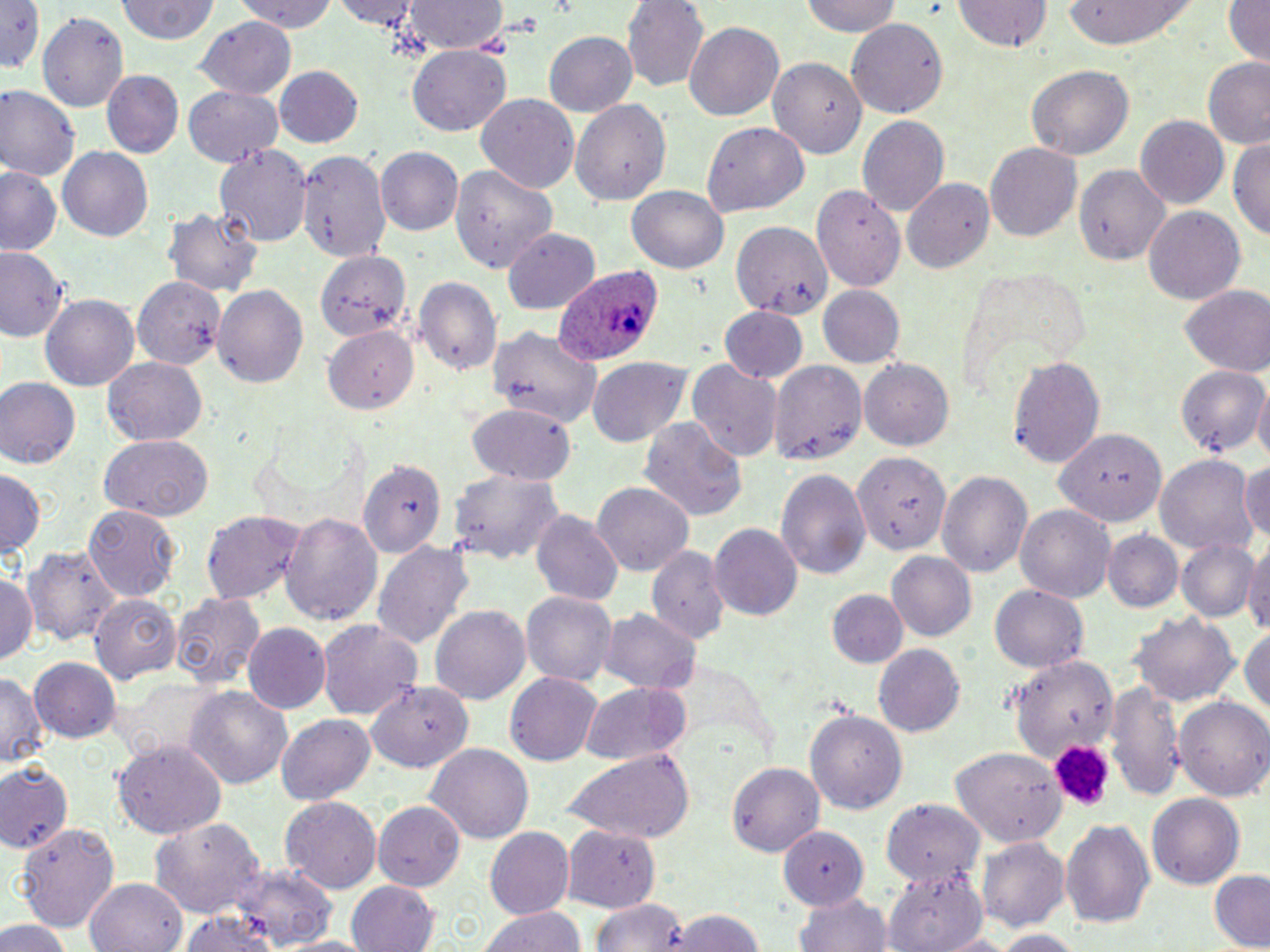

slide-level diagnosis = Plasmodium ovale
stain = May-Grünwald-Giemsa
magnification = 1000x
platelet locations = approximate bounding boxes as named x1/y1/x2/y2 corners in pixels: (x1=1050, y1=737, x2=1116, y2=807)
preparation = thin blood smear
field of view = single
uninfected red blood cell locations = approximate bounding boxes as named x1/y1/x2/y2 corners in pixels: (x1=231, y1=0, x2=341, y2=33), (x1=336, y1=0, x2=421, y2=32), (x1=406, y1=0, x2=508, y2=56), (x1=801, y1=0, x2=902, y2=39), (x1=957, y1=0, x2=1051, y2=55), (x1=1061, y1=0, x2=1200, y2=47), (x1=1221, y1=0, x2=1270, y2=65), (x1=115, y1=1, x2=220, y2=46), (x1=622, y1=1, x2=709, y2=90), (x1=0, y1=3, x2=48, y2=77), (x1=37, y1=12, x2=129, y2=113), (x1=196, y1=17, x2=295, y2=97), (x1=847, y1=18, x2=949, y2=116), (x1=685, y1=20, x2=784, y2=123), (x1=543, y1=31, x2=637, y2=117), (x1=407, y1=46, x2=513, y2=136), (x1=770, y1=58, x2=867, y2=162), (x1=1203, y1=60, x2=1270, y2=149), (x1=1025, y1=65, x2=1134, y2=161), (x1=272, y1=66, x2=365, y2=149), (x1=101, y1=71, x2=181, y2=156), (x1=0, y1=85, x2=82, y2=179), (x1=184, y1=85, x2=284, y2=167), (x1=476, y1=95, x2=579, y2=192), (x1=571, y1=98, x2=671, y2=206), (x1=858, y1=115, x2=949, y2=216), (x1=1136, y1=116, x2=1228, y2=208), (x1=702, y1=122, x2=807, y2=215), (x1=1231, y1=137, x2=1270, y2=243), (x1=215, y1=142, x2=311, y2=244), (x1=985, y1=143, x2=1084, y2=241), (x1=57, y1=146, x2=153, y2=242), (x1=375, y1=147, x2=463, y2=236), (x1=299, y1=148, x2=392, y2=258), (x1=450, y1=163, x2=555, y2=275), (x1=1074, y1=164, x2=1171, y2=267), (x1=0, y1=165, x2=63, y2=257), (x1=900, y1=178, x2=994, y2=275), (x1=627, y1=186, x2=730, y2=274), (x1=811, y1=187, x2=903, y2=293), (x1=165, y1=204, x2=263, y2=299), (x1=1143, y1=207, x2=1246, y2=303), (x1=730, y1=219, x2=831, y2=314), (x1=503, y1=228, x2=599, y2=310), (x1=0, y1=247, x2=68, y2=344), (x1=309, y1=247, x2=414, y2=344), (x1=133, y1=275, x2=226, y2=372), (x1=417, y1=276, x2=500, y2=377), (x1=213, y1=283, x2=308, y2=387), (x1=818, y1=286, x2=906, y2=368), (x1=1180, y1=288, x2=1268, y2=376), (x1=40, y1=294, x2=139, y2=393), (x1=720, y1=306, x2=810, y2=383), (x1=489, y1=324, x2=601, y2=433), (x1=325, y1=328, x2=417, y2=413), (x1=103, y1=355, x2=207, y2=446), (x1=1009, y1=355, x2=1105, y2=469), (x1=588, y1=357, x2=689, y2=448), (x1=860, y1=357, x2=957, y2=450), (x1=688, y1=358, x2=783, y2=464), (x1=770, y1=359, x2=867, y2=466), (x1=1177, y1=363, x2=1270, y2=457), (x1=0, y1=377, x2=79, y2=470), (x1=1252, y1=382, x2=1270, y2=466), (x1=465, y1=405, x2=576, y2=484), (x1=641, y1=417, x2=744, y2=524), (x1=1057, y1=427, x2=1167, y2=530), (x1=97, y1=436, x2=216, y2=520), (x1=855, y1=452, x2=949, y2=553), (x1=1154, y1=455, x2=1256, y2=555), (x1=1244, y1=457, x2=1270, y2=545), (x1=359, y1=458, x2=449, y2=559), (x1=775, y1=466, x2=871, y2=579), (x1=448, y1=467, x2=566, y2=566), (x1=1, y1=469, x2=44, y2=560), (x1=937, y1=469, x2=1033, y2=578), (x1=591, y1=481, x2=693, y2=577), (x1=85, y1=506, x2=180, y2=601), (x1=1016, y1=507, x2=1114, y2=601), (x1=532, y1=509, x2=624, y2=606), (x1=201, y1=511, x2=306, y2=605), (x1=280, y1=511, x2=382, y2=627), (x1=708, y1=521, x2=802, y2=618), (x1=1105, y1=530, x2=1182, y2=611), (x1=1177, y1=538, x2=1257, y2=623), (x1=1244, y1=538, x2=1270, y2=633), (x1=372, y1=540, x2=474, y2=651), (x1=24, y1=544, x2=118, y2=647), (x1=646, y1=546, x2=729, y2=646), (x1=885, y1=552, x2=975, y2=641), (x1=0, y1=572, x2=40, y2=666), (x1=991, y1=585, x2=1089, y2=671), (x1=828, y1=587, x2=907, y2=667), (x1=169, y1=590, x2=267, y2=689), (x1=521, y1=590, x2=617, y2=685), (x1=90, y1=594, x2=181, y2=683), (x1=431, y1=604, x2=530, y2=704), (x1=1133, y1=609, x2=1240, y2=707), (x1=598, y1=610, x2=700, y2=693), (x1=316, y1=616, x2=423, y2=721), (x1=242, y1=624, x2=329, y2=714), (x1=1242, y1=625, x2=1270, y2=722), (x1=873, y1=643, x2=964, y2=737), (x1=1005, y1=654, x2=1116, y2=758), (x1=30, y1=657, x2=121, y2=744), (x1=0, y1=671, x2=46, y2=769), (x1=504, y1=671, x2=602, y2=766), (x1=577, y1=680, x2=689, y2=767), (x1=1103, y1=680, x2=1187, y2=799), (x1=367, y1=681, x2=472, y2=775), (x1=186, y1=685, x2=293, y2=790), (x1=1174, y1=698, x2=1270, y2=800), (x1=805, y1=709, x2=909, y2=813), (x1=275, y1=713, x2=375, y2=804), (x1=113, y1=741, x2=228, y2=839), (x1=425, y1=743, x2=533, y2=845), (x1=559, y1=746, x2=697, y2=844), (x1=951, y1=747, x2=1067, y2=846), (x1=0, y1=762, x2=73, y2=856), (x1=727, y1=764, x2=823, y2=856), (x1=1148, y1=791, x2=1245, y2=887), (x1=282, y1=796, x2=381, y2=891), (x1=881, y1=798, x2=980, y2=883), (x1=374, y1=801, x2=464, y2=890), (x1=152, y1=816, x2=267, y2=923), (x1=774, y1=819, x2=874, y2=912), (x1=17, y1=821, x2=121, y2=933), (x1=1061, y1=821, x2=1155, y2=929), (x1=484, y1=827, x2=576, y2=919), (x1=562, y1=827, x2=658, y2=911), (x1=977, y1=837, x2=1069, y2=932), (x1=227, y1=867, x2=338, y2=946), (x1=885, y1=868, x2=988, y2=952), (x1=1210, y1=870, x2=1270, y2=950), (x1=86, y1=878, x2=185, y2=952), (x1=345, y1=881, x2=439, y2=952), (x1=793, y1=890, x2=895, y2=952), (x1=593, y1=897, x2=691, y2=951), (x1=478, y1=905, x2=587, y2=952), (x1=662, y1=906, x2=765, y2=952), (x1=177, y1=908, x2=289, y2=952), (x1=0, y1=919, x2=72, y2=952), (x1=988, y1=928, x2=1085, y2=952), (x1=935, y1=932, x2=1019, y2=952), (x1=278, y1=935, x2=379, y2=952)
Plasmodium ovale-infected red blood cell locations = approximate bounding boxes as named x1/y1/x2/y2 corners in pixels: (x1=555, y1=267, x2=660, y2=366)
image size = 1270×952 pixels
modality = light microscopy